Assess this cell for malaria.
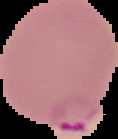
Parasitized.

Cell region segmented out of the field of view; the surrounding area is masked to black. Image is 118×139 pixels. From a thin blood film.